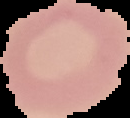
image size = 130×118 pixels
result = no malaria parasites detected
image type = segmented cell region on a black background
preparation = thin blood film